Report the malaria status of this cell.
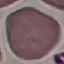
It is uninfected.

preparation: thin blood film
stain: Giemsa
capture: smartphone camera at the microscope eyepiece
image_type: cell patch, automatically extracted from a larger field of view and resized to 64 × 64 pixels